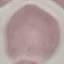 Malaria status: uninfected. Thin blood smear. Acquired by smartphone through the microscope eyepiece. Automatically extracted cell patch, resized to 64 × 64 pixels. Giemsa-stained preparation.